Identify the cell.
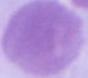
An erythrocyte.

Micrograph. 1000x magnification.